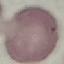

Summary:
  - Malaria status: uninfected
  - Stain: Giemsa
  - Image type: automatically extracted cell patch, resized to 64 × 64 pixels
  - Preparation: thin blood film
  - Capture: smartphone camera at the microscope eyepiece